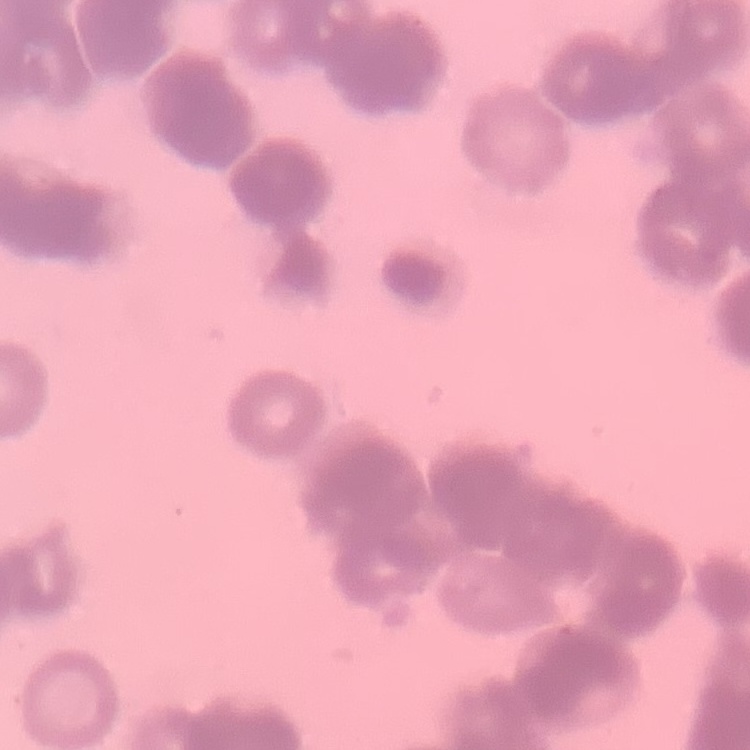
Summary:
  - Erythrocyte morphology: rouleaux formation
  - Preparation: thin peripheral smear
  - Stain: Field's or Giemsa
  - Image type: square crop of a larger photomicrograph